Give the position of every malaria parasite and every leukocyte.
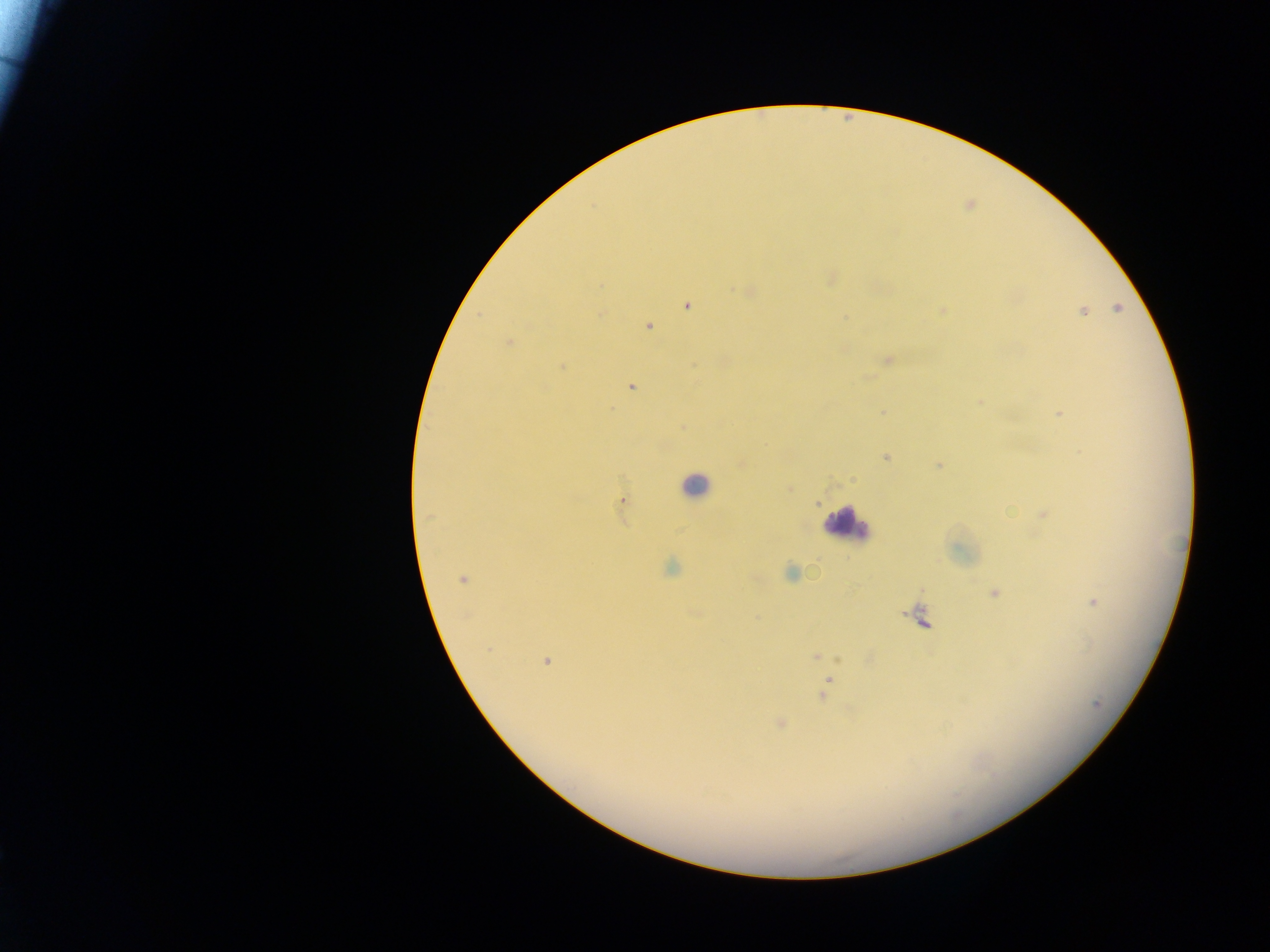

Approximate centers as (x, y) in pixels.
Malaria parasites: (748, 292), (687, 305), (1118, 308), (943, 310), (1083, 311), (845, 318), (649, 327), (509, 342), (887, 359), (563, 367), (631, 387), (980, 404), (883, 413), (1059, 413), (885, 458), (938, 467), (621, 500), (1044, 515), (429, 516), (671, 568), (790, 573), (462, 580), (994, 593), (1092, 602), (489, 651), (815, 657), (546, 661), (829, 680), (822, 696), (1098, 704), (780, 723).
Leukocytes: (695, 485), (847, 523).

One field of view. Image is 1270×952 pixels. Mobile-phone photograph taken through the microscope. Collected in Ghana. Thick blood film.